Locate platelets.
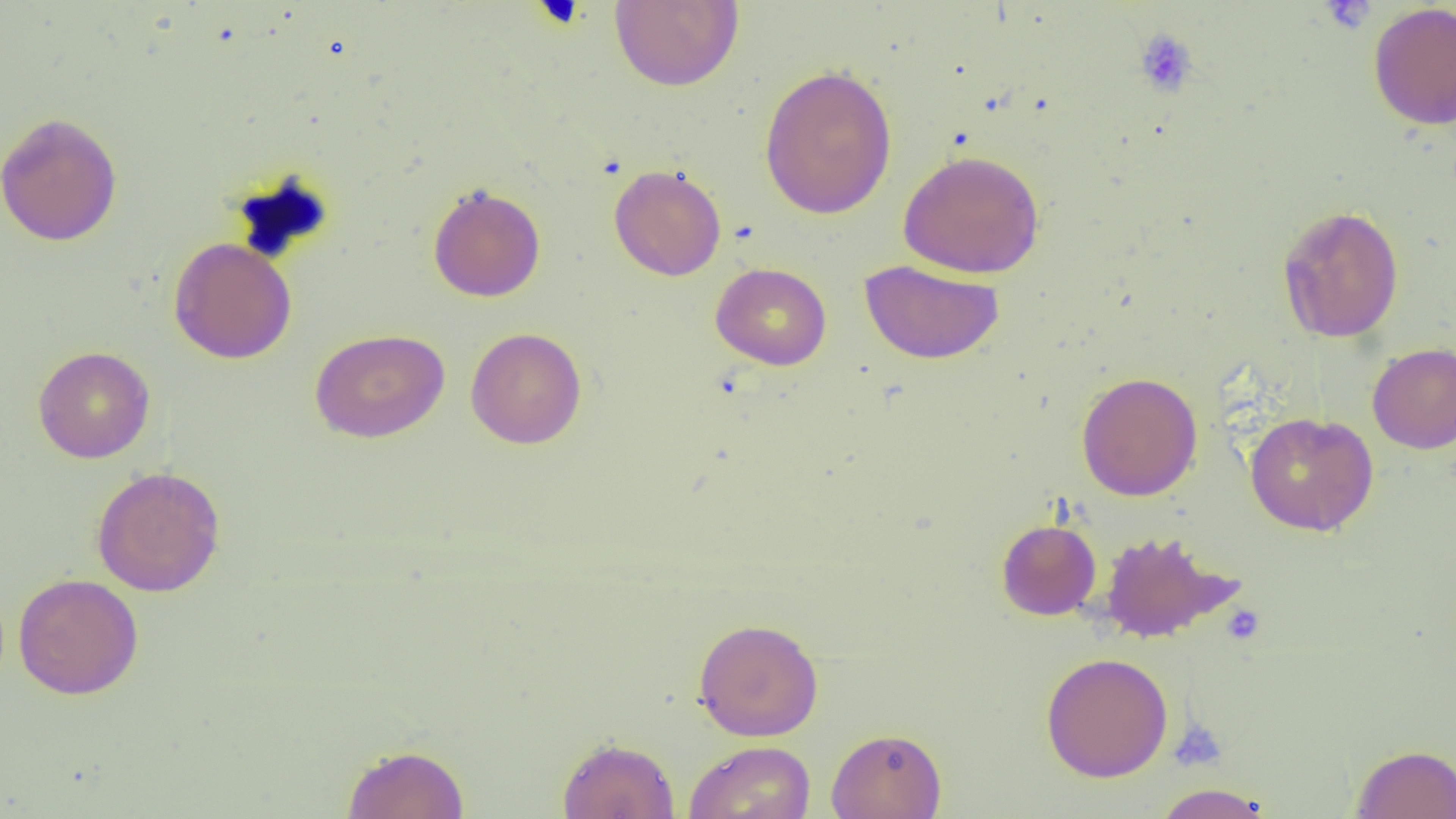

Approximate bounding boxes as named x1/y1/x2/y2 corners in pixels.
Platelets: (x1=1320, y1=1, x2=1375, y2=34), (x1=1133, y1=28, x2=1199, y2=98), (x1=1219, y1=602, x2=1266, y2=646), (x1=1168, y1=718, x2=1228, y2=772).

slide_level_diagnosis: no evidence of blood parasites
image_size: 1456×819 pixels
field_of_view: one of a larger specimen
magnification: 1000x
modality: light microscopy
preparation: thin blood film
uninfected_red_blood_cell_locations: 'approximate bounding boxes as named x1/y1/x2/y2 corners in pixels: (x1=609, y1=0, x2=744, y2=91), (x1=1367, y1=1, x2=1456, y2=131), (x1=759, y1=64, x2=898, y2=220), (x1=0, y1=111, x2=122, y2=247), (x1=897, y1=149, x2=1046, y2=278), (x1=609, y1=164, x2=726, y2=281), (x1=427, y1=183, x2=546, y2=302), (x1=1277, y1=205, x2=1405, y2=343), (x1=168, y1=237, x2=297, y2=364), (x1=860, y1=259, x2=1004, y2=364), (x1=710, y1=262, x2=832, y2=370), (x1=465, y1=327, x2=586, y2=449), (x1=310, y1=328, x2=449, y2=443), (x1=1367, y1=343, x2=1456, y2=454), (x1=33, y1=345, x2=155, y2=464), (x1=1076, y1=372, x2=1203, y2=501), (x1=1245, y1=411, x2=1378, y2=536), (x1=91, y1=465, x2=226, y2=597), (x1=996, y1=518, x2=1101, y2=620), (x1=1097, y1=530, x2=1243, y2=644), (x1=12, y1=573, x2=144, y2=700), (x1=693, y1=618, x2=823, y2=741), (x1=1040, y1=652, x2=1174, y2=782), (x1=825, y1=727, x2=947, y2=819), (x1=556, y1=736, x2=680, y2=818), (x1=683, y1=740, x2=816, y2=819), (x1=342, y1=743, x2=470, y2=819), (x1=1351, y1=744, x2=1456, y2=819), (x1=1152, y1=783, x2=1274, y2=818)'